Locate every blood parasite and identify its species.
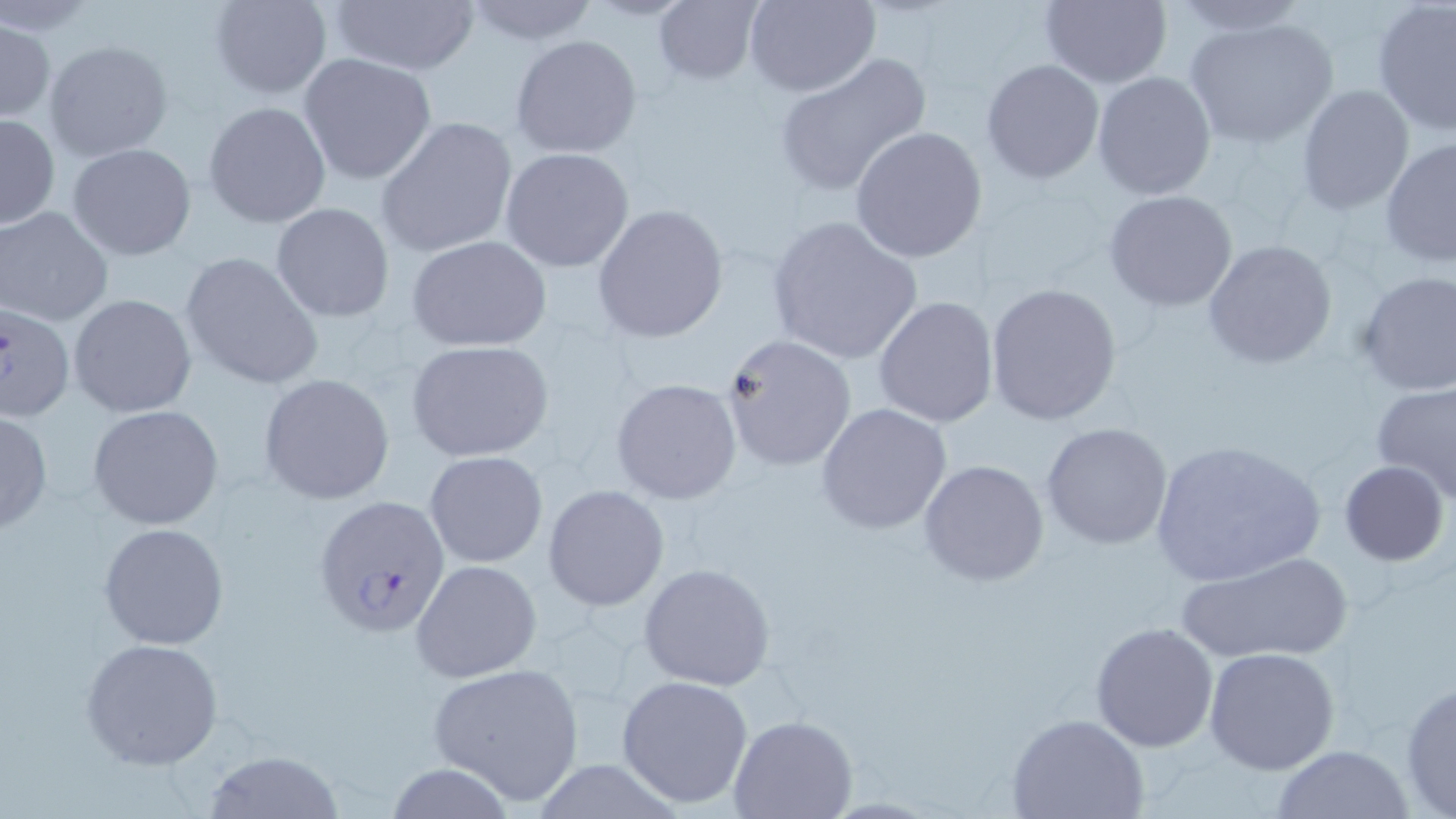

Approximate bounding boxes as [x1, y1, x2, y2] in pixels.
Plasmodium falciparum-infected red blood cells: [1, 299, 76, 423], [314, 494, 449, 637].
No Plasmodium ovale, Plasmodium malariae, Plasmodium vivax, Babesia divergens, or Trypanosoma brucei observed.

Summary:
  - Uninfected red blood cell locations: [210, 0, 331, 99], [327, 0, 481, 78], [459, 0, 601, 45], [653, 0, 763, 86], [744, 0, 879, 97], [1165, 0, 1313, 33], [1371, 0, 1455, 136], [1037, 1, 1172, 88], [1183, 16, 1338, 148], [1, 18, 54, 122], [509, 35, 642, 159], [44, 40, 173, 163], [299, 53, 437, 185], [774, 53, 931, 197], [981, 59, 1104, 183], [1092, 71, 1217, 199], [1294, 84, 1415, 214], [203, 101, 331, 228], [1, 113, 59, 230], [375, 116, 519, 259], [849, 127, 989, 264], [1380, 136, 1456, 270], [67, 143, 197, 262], [500, 147, 634, 273], [1102, 190, 1239, 312], [270, 201, 396, 323], [592, 204, 730, 343], [0, 206, 113, 326], [765, 215, 924, 366], [407, 234, 552, 351], [1203, 239, 1337, 371], [179, 251, 325, 391], [1354, 271, 1456, 396], [984, 282, 1124, 426], [67, 294, 197, 419], [873, 295, 999, 428], [720, 335, 856, 472], [404, 338, 555, 462], [258, 374, 398, 506], [610, 379, 742, 504], [1371, 381, 1456, 497], [816, 404, 953, 535], [86, 405, 226, 531], [0, 409, 52, 536], [1042, 421, 1173, 550], [1148, 439, 1327, 589], [423, 450, 549, 569], [919, 458, 1051, 588], [1339, 460, 1450, 566], [543, 486, 669, 611], [99, 522, 231, 651], [1178, 549, 1354, 665], [411, 559, 542, 682], [639, 563, 776, 691], [1090, 622, 1220, 751], [79, 637, 226, 771], [1204, 647, 1340, 776], [426, 662, 583, 803], [615, 674, 753, 808], [1400, 677, 1456, 816], [1008, 713, 1150, 819], [728, 715, 858, 819], [1267, 745, 1415, 818], [205, 749, 347, 819]
  - Slide-level diagnosis: Plasmodium falciparum
  - Image size: 1456×819 pixels
  - Modality: light microscopy
  - Magnification: 1000x
  - Preparation: thin blood film
  - Field of view: one of a larger specimen
  - Stain: May-Grünwald-Giemsa